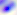 Toxoplasma gondii is seen. Micrograph. 400x magnification.